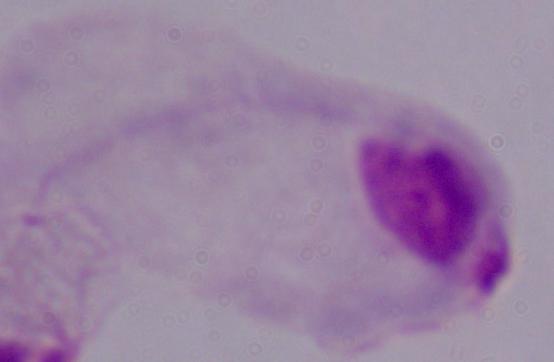
magnification = 1000x
identification = trichomonad
modality = photomicrograph